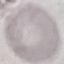

Malaria status: uninfected. Giemsa stain. Photographed with a smartphone camera at the microscope eyepiece. Cell patch, automatically extracted from a larger field of view and resized to 64 × 64 pixels. Thin blood film.